Outline each Plasmodium falciparum-infected red blood cell.
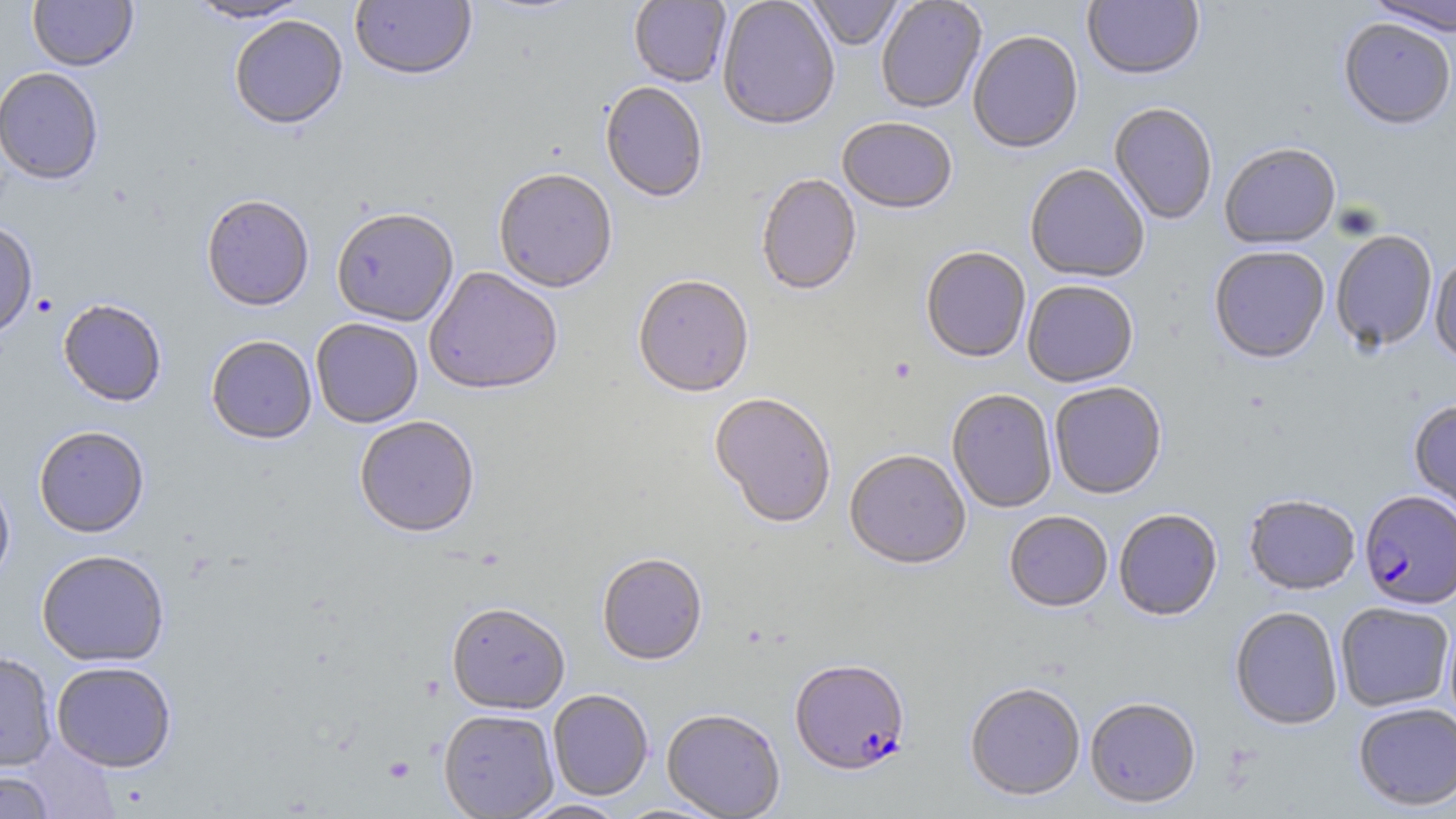

Approximate bounding boxes as [x1, y1, x2, y2] in pixels.
Plasmodium falciparum-infected red blood cells: [1360, 491, 1456, 609], [789, 660, 911, 777].

{
  "slide_level_diagnosis": "Plasmodium falciparum",
  "platelet_locations": "approximate bounding boxes as [x1, y1, x2, y2] in pixels: [383, 756, 416, 783]",
  "modality": "optical microscopy",
  "uninfected_red_blood_cell_locations": "approximate bounding boxes as [x1, y1, x2, y2] in pixels: [28, 0, 138, 72], [349, 0, 477, 84], [473, 0, 590, 19], [629, 0, 731, 88], [717, 0, 840, 133], [805, 0, 903, 52], [876, 0, 987, 114], [1083, 0, 1204, 83], [1364, 0, 1456, 37], [185, 1, 314, 24], [229, 15, 348, 130], [1338, 20, 1455, 132], [968, 32, 1084, 157], [0, 66, 104, 185], [599, 83, 707, 204], [1109, 104, 1217, 226], [837, 119, 957, 216], [1219, 144, 1341, 251], [1025, 165, 1150, 285], [493, 171, 618, 295], [756, 175, 861, 298], [201, 196, 314, 312], [332, 211, 459, 328], [0, 220, 38, 339], [1331, 233, 1437, 354], [1209, 248, 1330, 365], [921, 249, 1031, 365], [1429, 253, 1456, 368], [424, 268, 563, 398], [633, 277, 754, 400], [1022, 281, 1138, 389], [57, 299, 167, 407], [311, 319, 424, 429], [205, 336, 318, 446], [1049, 383, 1167, 500], [947, 390, 1057, 514], [709, 394, 836, 530], [1408, 399, 1456, 520], [355, 418, 480, 539], [33, 426, 149, 538], [845, 452, 971, 572], [0, 473, 15, 591], [1244, 495, 1360, 596], [1114, 510, 1222, 622], [1004, 512, 1113, 614], [36, 549, 170, 667], [597, 555, 707, 667], [1335, 602, 1454, 712], [446, 604, 570, 716], [1229, 607, 1343, 731], [1444, 614, 1456, 736], [0, 651, 57, 771], [51, 661, 177, 773], [964, 684, 1085, 802], [548, 690, 654, 801], [1085, 698, 1201, 810], [1353, 702, 1456, 811], [662, 709, 786, 819], [439, 710, 559, 819], [0, 771, 55, 819], [516, 799, 628, 818]",
  "image_size": "1456×819 pixels",
  "magnification": "1000x",
  "stain": "May-Grünwald-Giemsa",
  "field_of_view": "single",
  "preparation": "thin blood smear"
}